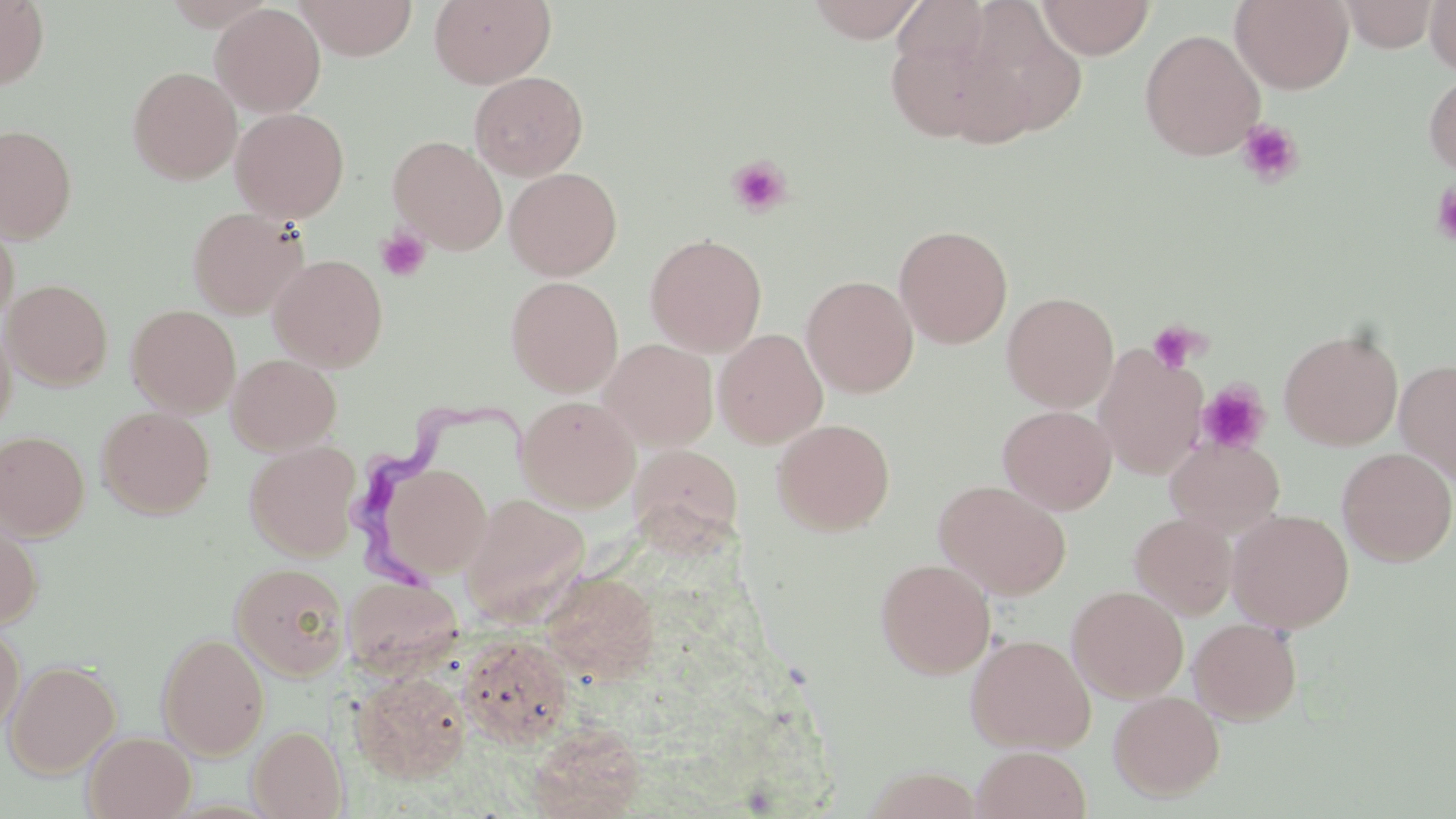
slide_level_diagnosis: Trypanosoma brucei
image_size: 1456×819 pixels
trypanosoma_brucei_locations: 'approximate bounding boxes as (x1, y1, x2, y2) in pixels: (344, 400, 534, 595)'
preparation: thin blood film
magnification: 1000x
stain: May-Grünwald-Giemsa
modality: optical microscopy
field_of_view: single
platelet_locations: 'approximate bounding boxes as (x1, y1, x2, y2) in pixels: (1236, 119, 1304, 188), (727, 156, 792, 217), (1430, 181, 1456, 247), (376, 227, 430, 281), (1145, 319, 1206, 374), (1196, 380, 1272, 455)'
uninfected_red_blood_cell_locations: 'approximate bounding boxes as (x1, y1, x2, y2) in pixels: (0, 0, 50, 89), (295, 0, 418, 60), (429, 0, 556, 89), (806, 0, 928, 42), (892, 0, 992, 68), (1037, 0, 1155, 59), (1230, 0, 1354, 94), (1340, 0, 1439, 52), (1424, 0, 1456, 75), (210, 3, 326, 117), (954, 5, 1089, 143), (884, 23, 1012, 145), (1140, 28, 1265, 161), (127, 66, 242, 185), (1423, 69, 1456, 180), (469, 71, 588, 180), (230, 107, 350, 224), (0, 124, 78, 243), (389, 135, 507, 253), (504, 167, 623, 280), (188, 206, 307, 319), (0, 216, 19, 327), (894, 224, 1013, 348), (645, 233, 767, 356), (268, 253, 388, 372), (801, 275, 919, 397), (505, 276, 624, 395), (3, 279, 113, 390), (1002, 291, 1119, 412), (126, 304, 241, 417), (0, 315, 16, 441), (1279, 327, 1403, 450), (714, 328, 828, 448), (601, 339, 718, 450), (1095, 344, 1208, 479), (227, 353, 342, 454), (1395, 359, 1456, 484), (516, 395, 640, 512), (997, 404, 1117, 515), (97, 406, 214, 518), (772, 418, 895, 535), (0, 430, 90, 540), (1166, 437, 1285, 536), (244, 440, 362, 560), (628, 444, 744, 553), (1336, 448, 1456, 566), (374, 462, 493, 580), (933, 479, 1072, 600), (459, 493, 590, 621), (1228, 507, 1354, 632), (0, 512, 42, 631), (1129, 512, 1237, 619), (875, 558, 995, 679), (231, 562, 349, 681), (541, 569, 661, 684), (344, 575, 463, 675), (1067, 585, 1189, 702), (1188, 618, 1303, 725), (0, 621, 26, 740), (156, 632, 270, 759), (457, 633, 574, 748), (966, 633, 1096, 754), (5, 659, 122, 778), (351, 671, 471, 784), (1108, 690, 1225, 801), (527, 723, 646, 818), (248, 725, 347, 818), (83, 731, 196, 818), (972, 745, 1092, 819)'